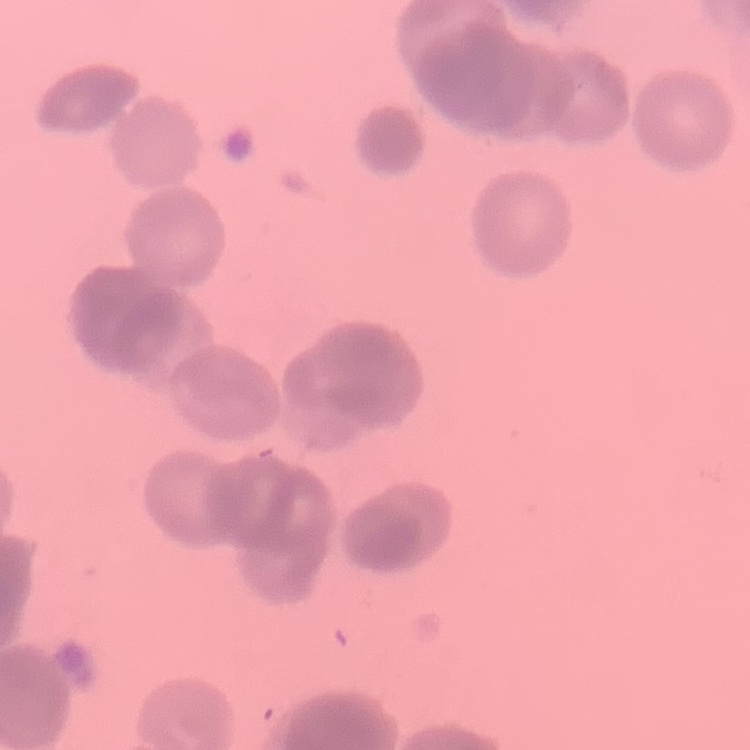

Summary:
  - Red blood cell morphology: rouleaux formation
  - Preparation: thin blood smear
  - Stain: Field's or Giemsa
  - Image type: one tile cut from a larger photomicrograph